State which parasite is depicted.
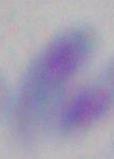

Toxoplasma gondii.

magnification = 1000x
modality = photomicrograph